State the blood parasite species.
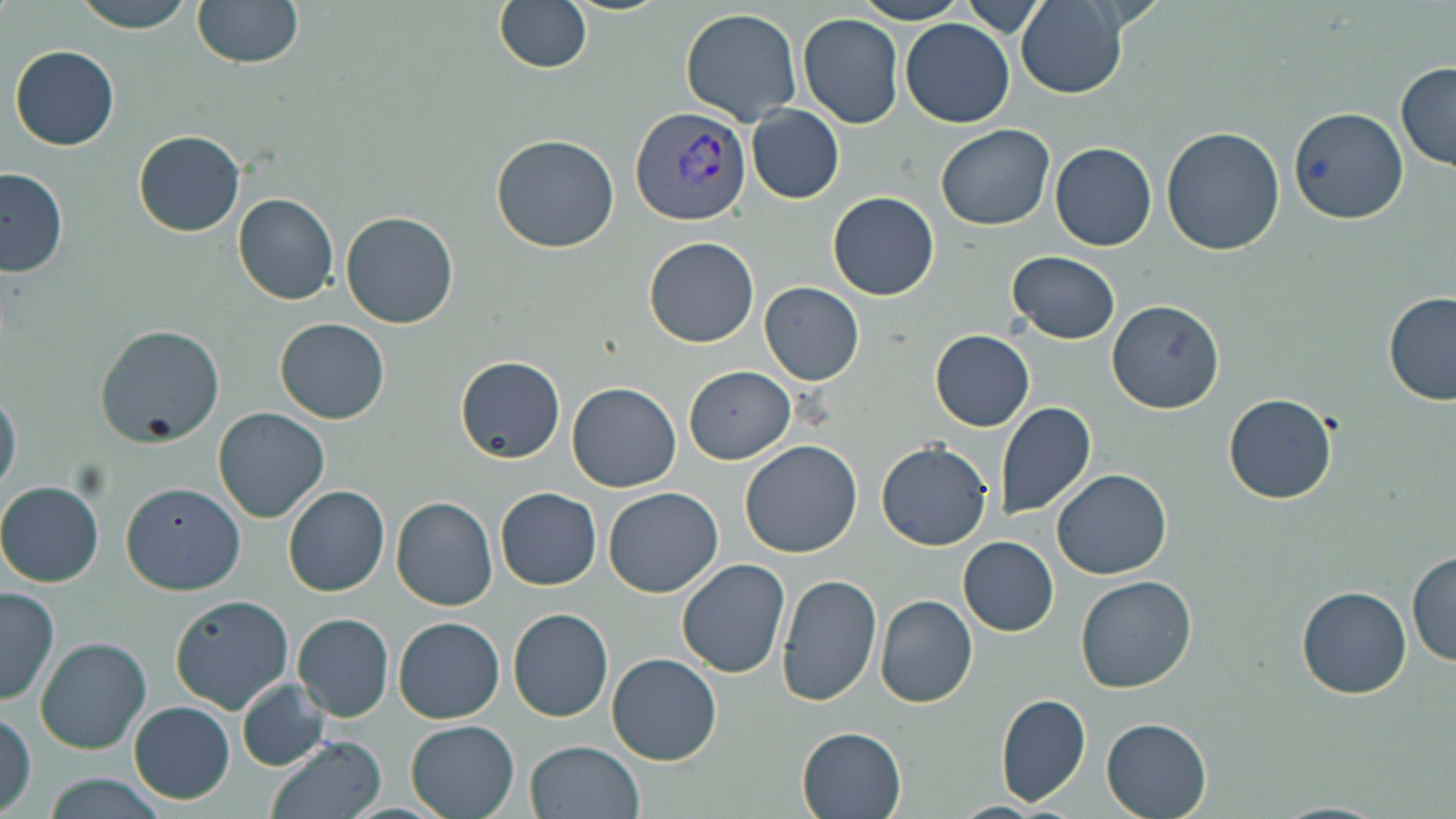

Plasmodium vivax.

preparation = thin blood film
Plasmodium vivax-infected red blood cell locations = approximate bounding boxes as named x1/y1/x2/y2 corners in pixels: (x1=632, y1=106, x2=753, y2=227)
image size = 1456×819 pixels
stain = May-Grünwald-Giemsa
magnification = 1000x
modality = light microscopy
uninfected red blood cell locations = approximate bounding boxes as named x1/y1/x2/y2 corners in pixels: (x1=73, y1=0, x2=197, y2=32), (x1=192, y1=0, x2=305, y2=69), (x1=494, y1=0, x2=592, y2=73), (x1=854, y1=1, x2=968, y2=24), (x1=1016, y1=1, x2=1128, y2=99), (x1=957, y1=3, x2=1050, y2=36), (x1=679, y1=9, x2=802, y2=126), (x1=798, y1=12, x2=904, y2=128), (x1=901, y1=17, x2=1014, y2=128), (x1=9, y1=44, x2=120, y2=151), (x1=1396, y1=64, x2=1456, y2=170), (x1=747, y1=105, x2=844, y2=204), (x1=1290, y1=107, x2=1408, y2=225), (x1=935, y1=125, x2=1055, y2=230), (x1=1161, y1=127, x2=1285, y2=255), (x1=133, y1=129, x2=245, y2=237), (x1=491, y1=135, x2=621, y2=254), (x1=1049, y1=142, x2=1158, y2=251), (x1=0, y1=166, x2=68, y2=276), (x1=827, y1=192, x2=939, y2=301), (x1=232, y1=194, x2=340, y2=305), (x1=340, y1=210, x2=459, y2=328), (x1=644, y1=236, x2=759, y2=348), (x1=1007, y1=251, x2=1120, y2=343), (x1=759, y1=283, x2=864, y2=385), (x1=1384, y1=292, x2=1456, y2=405), (x1=1106, y1=300, x2=1224, y2=414), (x1=276, y1=318, x2=389, y2=424), (x1=95, y1=324, x2=225, y2=447), (x1=929, y1=329, x2=1034, y2=431), (x1=456, y1=356, x2=566, y2=464), (x1=683, y1=365, x2=795, y2=464), (x1=567, y1=382, x2=681, y2=493), (x1=0, y1=389, x2=22, y2=497), (x1=1224, y1=394, x2=1336, y2=505), (x1=994, y1=402, x2=1096, y2=520), (x1=213, y1=407, x2=330, y2=524), (x1=740, y1=439, x2=862, y2=558), (x1=877, y1=441, x2=993, y2=551), (x1=1052, y1=468, x2=1172, y2=579), (x1=0, y1=480, x2=105, y2=588), (x1=121, y1=483, x2=245, y2=596), (x1=282, y1=487, x2=390, y2=597), (x1=603, y1=487, x2=724, y2=597), (x1=495, y1=488, x2=601, y2=590), (x1=391, y1=495, x2=498, y2=611), (x1=957, y1=536, x2=1058, y2=636), (x1=1406, y1=552, x2=1456, y2=668), (x1=676, y1=557, x2=790, y2=677), (x1=777, y1=572, x2=882, y2=705), (x1=1076, y1=575, x2=1198, y2=693), (x1=1297, y1=585, x2=1412, y2=698), (x1=0, y1=586, x2=59, y2=706), (x1=169, y1=595, x2=293, y2=714), (x1=875, y1=595, x2=979, y2=707), (x1=507, y1=607, x2=613, y2=722), (x1=292, y1=613, x2=394, y2=721), (x1=394, y1=617, x2=504, y2=724), (x1=35, y1=638, x2=152, y2=755), (x1=607, y1=652, x2=721, y2=765), (x1=237, y1=680, x2=329, y2=771), (x1=996, y1=693, x2=1091, y2=807), (x1=129, y1=701, x2=235, y2=804), (x1=1, y1=708, x2=37, y2=815), (x1=1100, y1=716, x2=1213, y2=819), (x1=403, y1=718, x2=521, y2=819), (x1=797, y1=726, x2=907, y2=818), (x1=264, y1=735, x2=387, y2=819), (x1=524, y1=740, x2=644, y2=819), (x1=41, y1=775, x2=167, y2=818)
field of view = one of a larger specimen